Identify the parasite.
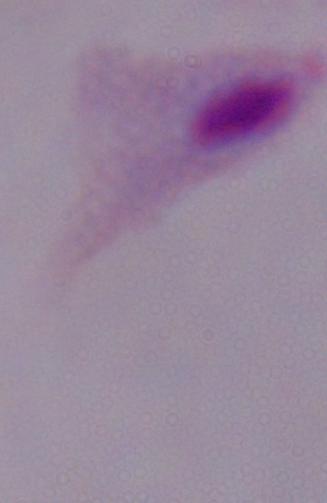

A trichomonad.

magnification = 1000x
modality = photomicrograph